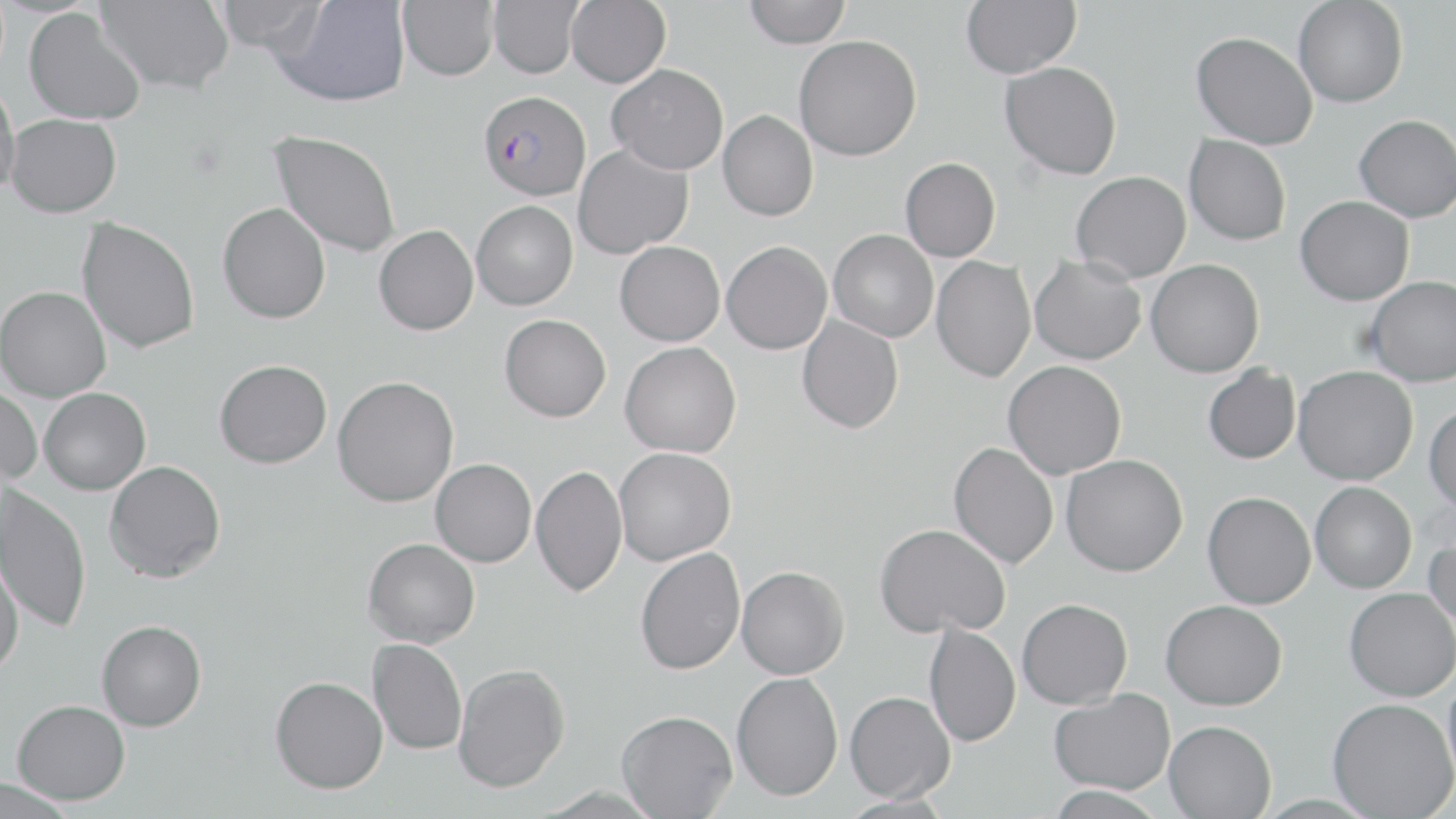

Approximate bounding boxes as (x1, y1, x2, y2) in pixels. Uninfected red blood cell locations: (96, 0, 234, 93), (488, 0, 583, 78), (566, 0, 670, 87), (743, 0, 851, 48), (960, 0, 1081, 78), (1293, 0, 1408, 107), (213, 1, 325, 52), (274, 1, 410, 106), (397, 1, 498, 81), (24, 8, 146, 125), (1191, 31, 1317, 149), (794, 34, 922, 161), (999, 61, 1122, 179), (607, 63, 728, 174), (0, 82, 20, 199), (718, 109, 818, 221), (6, 113, 121, 217), (1354, 115, 1456, 221), (270, 130, 400, 258), (1184, 134, 1291, 245), (573, 144, 693, 259), (900, 157, 1001, 262), (1071, 171, 1191, 283), (1295, 196, 1414, 305), (471, 200, 577, 310), (217, 203, 331, 324), (77, 217, 200, 353), (373, 224, 478, 335), (829, 229, 938, 342), (615, 240, 725, 345), (722, 241, 832, 354), (1030, 254, 1146, 365), (931, 255, 1036, 382), (1146, 258, 1264, 377), (1365, 276, 1456, 386), (0, 286, 111, 401), (499, 314, 611, 421), (797, 316, 904, 433), (620, 341, 741, 457), (215, 359, 332, 468), (1003, 360, 1126, 479), (1202, 364, 1300, 464), (1294, 365, 1418, 484), (332, 376, 459, 507), (0, 382, 43, 485), (39, 387, 150, 495), (1424, 404, 1456, 514), (949, 441, 1058, 569), (614, 447, 736, 565), (1061, 454, 1187, 576), (431, 458, 536, 567), (104, 460, 226, 582), (531, 464, 628, 597), (1310, 482, 1416, 592), (0, 485, 92, 633), (1203, 491, 1316, 608), (874, 523, 1010, 638), (1424, 527, 1456, 640), (363, 538, 480, 647), (636, 547, 746, 675), (0, 549, 25, 679), (736, 566, 849, 679), (1344, 587, 1456, 701), (1017, 598, 1132, 708), (1161, 599, 1287, 709), (96, 619, 207, 731), (924, 621, 1021, 747), (367, 638, 467, 755), (453, 662, 569, 793), (1443, 668, 1456, 796), (731, 672, 843, 801), (270, 675, 387, 793), (1049, 688, 1174, 795), (845, 690, 955, 802), (1328, 697, 1456, 819), (12, 699, 130, 805), (616, 709, 737, 818), (1163, 720, 1277, 818), (0, 777, 74, 819), (1046, 785, 1166, 818). Plasmodium falciparum-infected red blood cell locations: (478, 91, 591, 200). Slide-level diagnosis: Plasmodium falciparum. Thin blood smear. Single field of view. Light microscopy. Image is 1456×819 pixels. May-Grünwald-Giemsa stain. 1000x magnification.